Comment on the morphology of the erythrocytes.
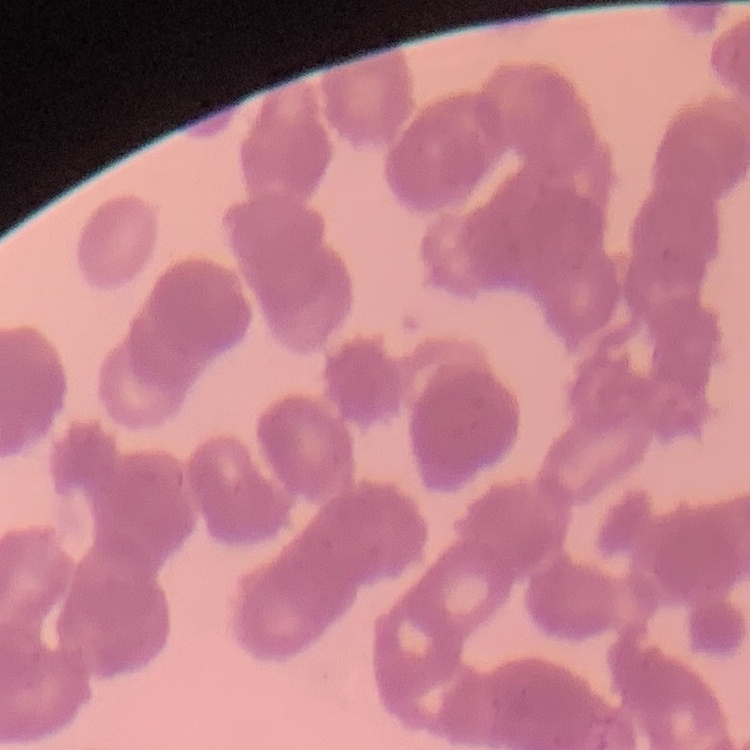

Rouleaux formation.

Thin peripheral smear. One tile cut from a larger photomicrograph. Stained with either Field's or Giemsa.